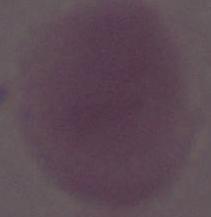

Summary:
  - Modality: micrograph
  - Identification: erythrocyte
  - Magnification: 1000x